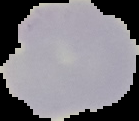
Result: no malaria parasites detected. Image is 139×121 pixels. The area outside the segmented cell region is set to black. From a thin blood smear.